State which parasite is depicted.
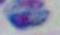

This is Toxoplasma gondii.

{
  "modality": "photomicrograph",
  "magnification": "1000x"
}